Report the malaria status of this cell.
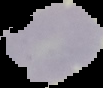
It is uninfected.

Summary:
  - Preparation: thin blood smear
  - Image type: segmented cell region with the area outside set to black
  - Image size: 103×88 pixels